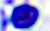 Captured at 400x magnification. Photomicrograph. A leukocyte is seen.